Identify the parasite.
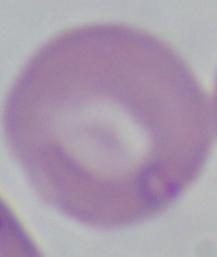

This is Babesia.

magnification = 1000x
modality = micrograph